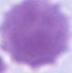

{
  "identification": "red blood cell",
  "magnification": "1000x",
  "modality": "photomicrograph"
}